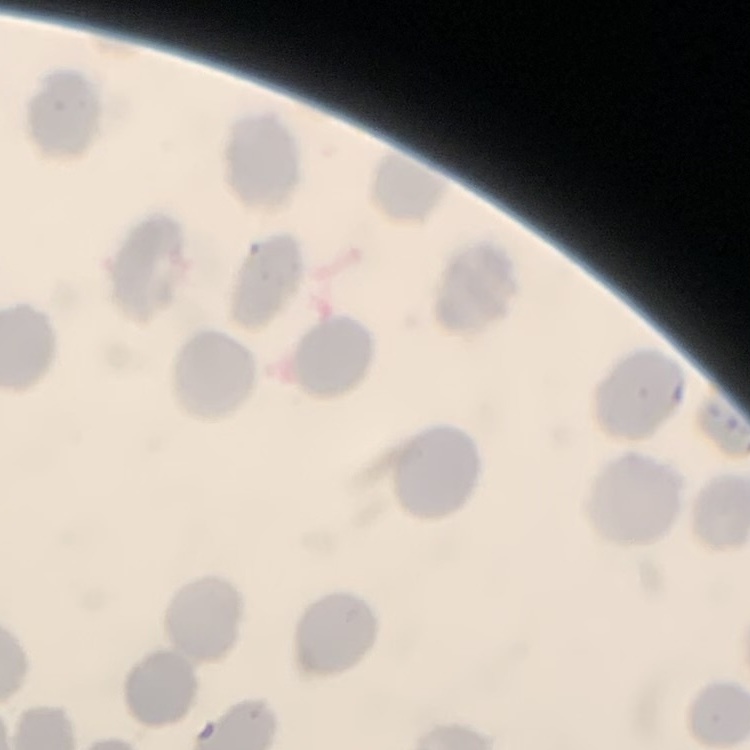

The red blood cells exhibit no rouleaux formation. Thin blood smear. Stained with either Field's or Giemsa. One tile cut from a larger photomicrograph.